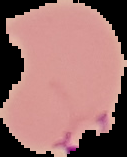 From a thin blood smear. Image is 127×157 pixels. Result: Plasmodium parasites identified. The area outside the segmented cell region is set to black.